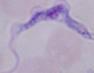
modality = photomicrograph
magnification = 1000x
identification = trypanosome